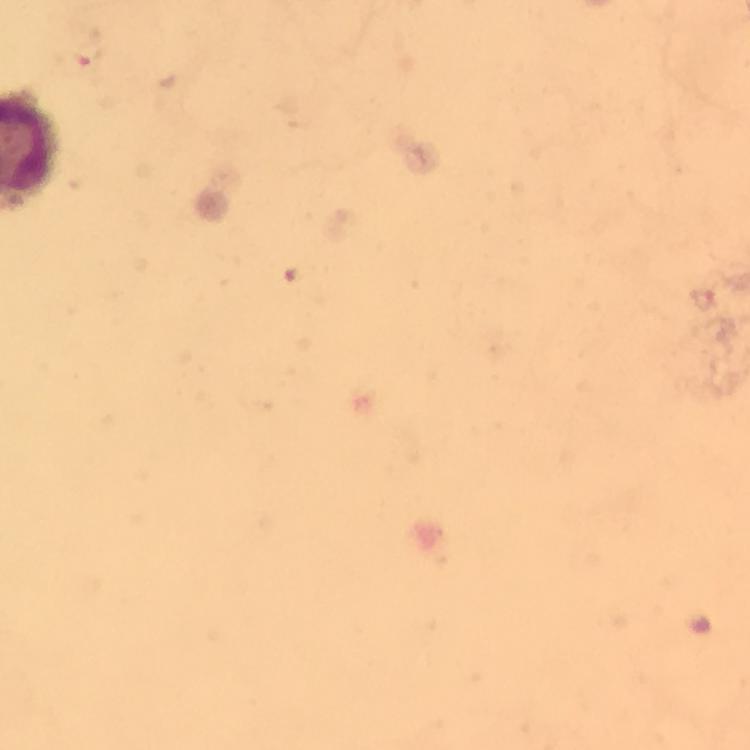
Approximate centers as [x, y] in pixels. Plasmodium parasite locations: [85, 53]. 100x magnification. Image is 750×750 pixels. Photographed with a smartphone mounted on the microscope. Giemsa stain. Immersion oil applied. Thick blood film. A crop from one field of view. From a diagnostic examination for malaria.